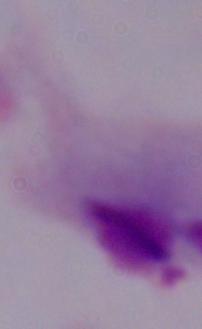
Summary:
  - Modality: micrograph
  - Magnification: 1000x
  - Identification: trichomonad